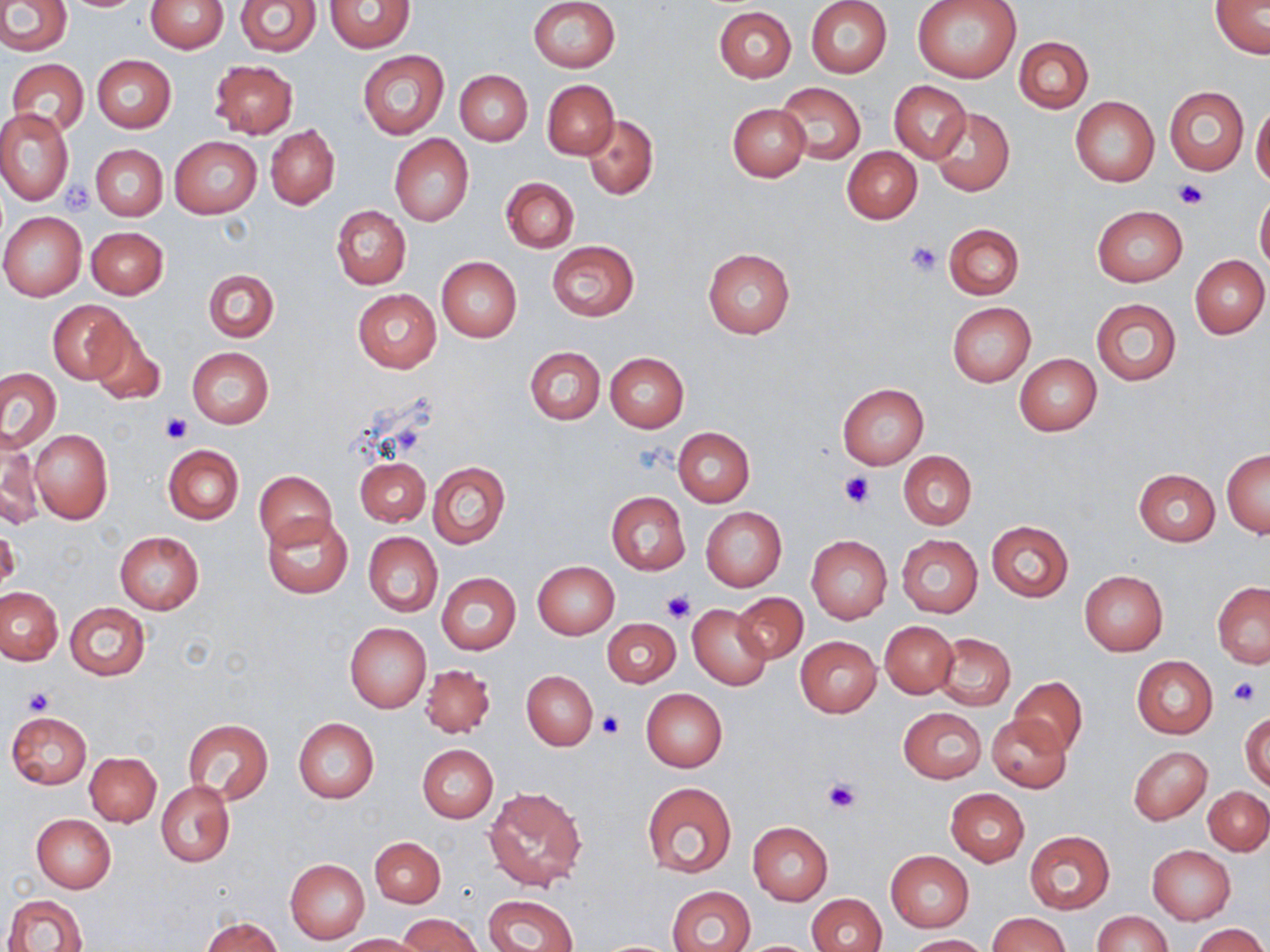
Summary:
  - Coordinate format: approximate bounding boxes as named x1/y1/x2/y2 corners in pixels
  - Platelet locations: (x1=1171, y1=178, x2=1208, y2=209), (x1=63, y1=182, x2=96, y2=214), (x1=906, y1=241, x2=942, y2=277), (x1=162, y1=415, x2=193, y2=444), (x1=840, y1=471, x2=874, y2=507), (x1=662, y1=589, x2=695, y2=622), (x1=1230, y1=678, x2=1259, y2=707), (x1=23, y1=687, x2=56, y2=716), (x1=597, y1=711, x2=625, y2=738), (x1=822, y1=777, x2=862, y2=814)
  - Uninfected red blood cell locations: (x1=0, y1=0, x2=70, y2=55), (x1=145, y1=0, x2=227, y2=53), (x1=529, y1=0, x2=619, y2=73), (x1=805, y1=0, x2=893, y2=78), (x1=913, y1=0, x2=1022, y2=82), (x1=234, y1=1, x2=320, y2=56), (x1=325, y1=1, x2=414, y2=52), (x1=1210, y1=2, x2=1269, y2=58), (x1=714, y1=6, x2=796, y2=82), (x1=1014, y1=36, x2=1093, y2=114), (x1=357, y1=51, x2=449, y2=139), (x1=92, y1=55, x2=176, y2=132), (x1=8, y1=58, x2=89, y2=136), (x1=209, y1=59, x2=297, y2=139), (x1=455, y1=69, x2=533, y2=145), (x1=542, y1=79, x2=618, y2=159), (x1=889, y1=80, x2=971, y2=163), (x1=774, y1=81, x2=867, y2=166), (x1=1164, y1=85, x2=1248, y2=176), (x1=1070, y1=96, x2=1159, y2=186), (x1=727, y1=102, x2=811, y2=182), (x1=1251, y1=106, x2=1270, y2=187), (x1=928, y1=107, x2=1015, y2=198), (x1=0, y1=108, x2=73, y2=205), (x1=582, y1=115, x2=657, y2=199), (x1=266, y1=125, x2=339, y2=209), (x1=390, y1=134, x2=473, y2=226), (x1=170, y1=137, x2=263, y2=218), (x1=91, y1=144, x2=168, y2=221), (x1=843, y1=148, x2=922, y2=224), (x1=502, y1=178, x2=578, y2=252), (x1=1255, y1=192, x2=1270, y2=273), (x1=331, y1=205, x2=411, y2=289), (x1=1092, y1=205, x2=1187, y2=286), (x1=0, y1=212, x2=86, y2=301), (x1=943, y1=222, x2=1024, y2=299), (x1=87, y1=227, x2=169, y2=299), (x1=547, y1=241, x2=639, y2=321), (x1=702, y1=247, x2=795, y2=339), (x1=1190, y1=255, x2=1269, y2=339), (x1=436, y1=256, x2=522, y2=342), (x1=204, y1=269, x2=278, y2=342), (x1=353, y1=289, x2=442, y2=372), (x1=1090, y1=297, x2=1182, y2=386), (x1=48, y1=300, x2=133, y2=385), (x1=947, y1=302, x2=1035, y2=386), (x1=87, y1=322, x2=165, y2=407), (x1=187, y1=347, x2=274, y2=428), (x1=525, y1=347, x2=604, y2=424), (x1=605, y1=352, x2=689, y2=432), (x1=1014, y1=353, x2=1102, y2=436), (x1=0, y1=368, x2=61, y2=451), (x1=838, y1=383, x2=928, y2=468), (x1=673, y1=427, x2=755, y2=507), (x1=29, y1=429, x2=113, y2=523), (x1=0, y1=430, x2=41, y2=530), (x1=163, y1=445, x2=243, y2=525), (x1=1222, y1=449, x2=1269, y2=537), (x1=898, y1=451, x2=977, y2=529), (x1=355, y1=456, x2=430, y2=527), (x1=429, y1=462, x2=510, y2=548), (x1=1134, y1=468, x2=1219, y2=545), (x1=254, y1=470, x2=336, y2=550), (x1=606, y1=491, x2=689, y2=576), (x1=700, y1=507, x2=786, y2=592), (x1=262, y1=514, x2=353, y2=599), (x1=985, y1=521, x2=1074, y2=602), (x1=1, y1=526, x2=20, y2=591), (x1=115, y1=531, x2=203, y2=612), (x1=363, y1=532, x2=442, y2=616), (x1=806, y1=535, x2=892, y2=623), (x1=897, y1=535, x2=982, y2=617), (x1=533, y1=561, x2=619, y2=639), (x1=1079, y1=571, x2=1168, y2=656), (x1=437, y1=573, x2=521, y2=654), (x1=1212, y1=582, x2=1270, y2=667), (x1=0, y1=586, x2=64, y2=664), (x1=732, y1=592, x2=807, y2=664), (x1=65, y1=602, x2=148, y2=681), (x1=688, y1=603, x2=773, y2=690), (x1=602, y1=618, x2=679, y2=688), (x1=879, y1=621, x2=958, y2=698), (x1=345, y1=622, x2=430, y2=712), (x1=935, y1=632, x2=1015, y2=709), (x1=795, y1=636, x2=882, y2=718), (x1=1132, y1=655, x2=1218, y2=738), (x1=420, y1=664, x2=495, y2=737), (x1=521, y1=670, x2=598, y2=751), (x1=1010, y1=676, x2=1086, y2=756), (x1=641, y1=688, x2=728, y2=771), (x1=899, y1=707, x2=986, y2=783), (x1=8, y1=712, x2=91, y2=788), (x1=1241, y1=712, x2=1269, y2=792), (x1=986, y1=714, x2=1071, y2=793), (x1=294, y1=718, x2=379, y2=802), (x1=183, y1=719, x2=273, y2=804), (x1=417, y1=744, x2=498, y2=822), (x1=1129, y1=746, x2=1212, y2=823), (x1=85, y1=752, x2=161, y2=825), (x1=156, y1=782, x2=234, y2=866), (x1=641, y1=782, x2=738, y2=879), (x1=483, y1=785, x2=588, y2=890), (x1=1203, y1=786, x2=1269, y2=854), (x1=946, y1=789, x2=1028, y2=867), (x1=31, y1=814, x2=115, y2=893), (x1=747, y1=821, x2=833, y2=905), (x1=1023, y1=831, x2=1114, y2=914), (x1=371, y1=836, x2=445, y2=909), (x1=1148, y1=845, x2=1236, y2=924), (x1=886, y1=850, x2=974, y2=932), (x1=285, y1=859, x2=370, y2=943), (x1=668, y1=886, x2=756, y2=952), (x1=805, y1=893, x2=886, y2=952), (x1=3, y1=894, x2=87, y2=952), (x1=484, y1=894, x2=578, y2=952), (x1=1093, y1=911, x2=1171, y2=952), (x1=989, y1=912, x2=1069, y2=952), (x1=399, y1=915, x2=481, y2=952), (x1=202, y1=916, x2=282, y2=952), (x1=1192, y1=924, x2=1268, y2=952), (x1=339, y1=933, x2=427, y2=952), (x1=904, y1=934, x2=989, y2=952)
  - Slide-level diagnosis: no evidence of blood parasites
  - Field of view: single
  - Stain: May-Grünwald-Giemsa
  - Preparation: thin blood film
  - Image size: 1270×952 pixels
  - Magnification: 1000x
  - Modality: light microscopy